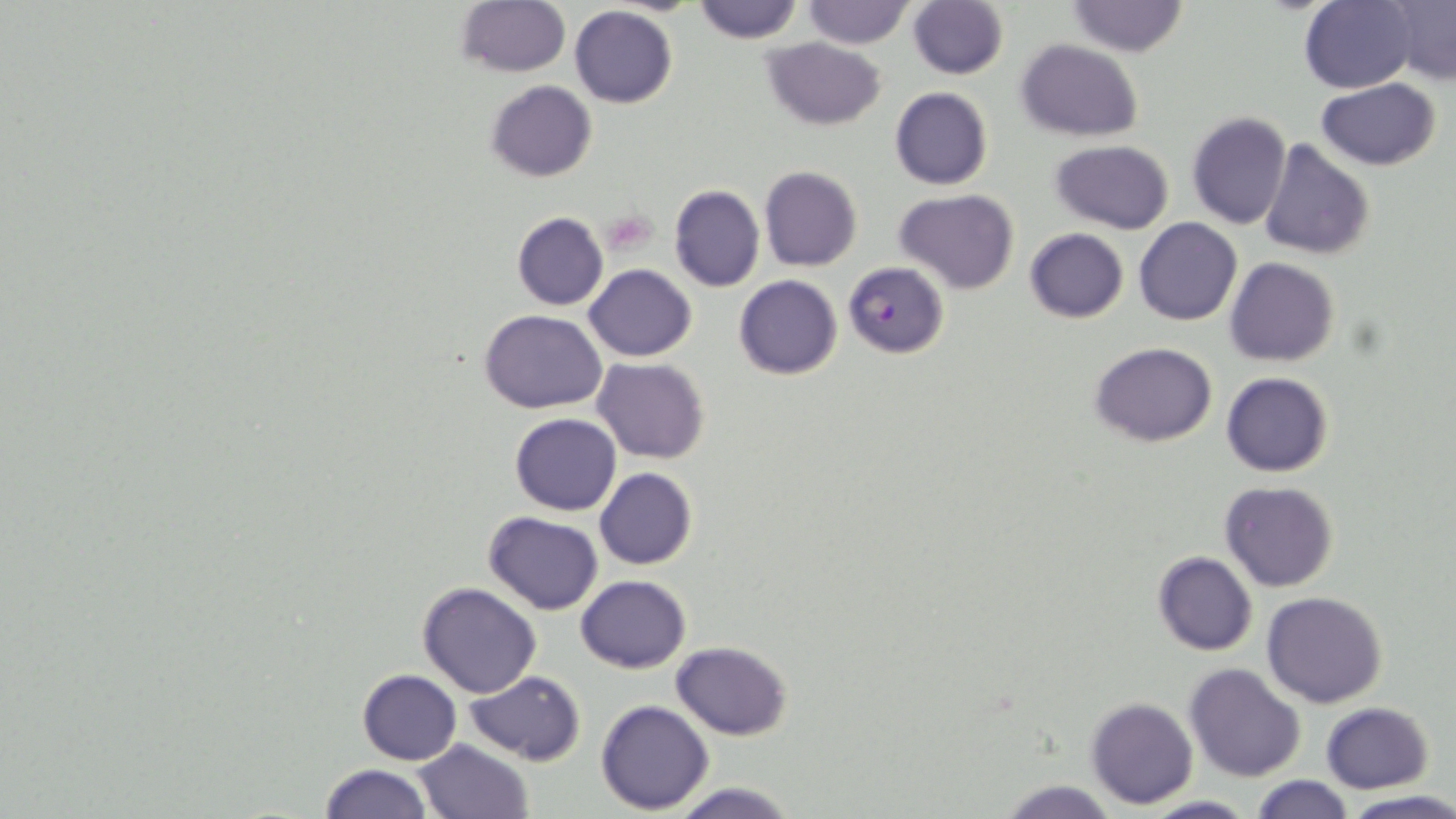

Summary:
  - Coordinate format: approximate bounding boxes as [x1, y1, x2, y2] in pixels
  - Uninfected red blood cell locations: [455, 0, 570, 79], [691, 0, 804, 43], [799, 0, 914, 47], [908, 0, 1007, 79], [1301, 0, 1418, 93], [1383, 0, 1456, 86], [1065, 1, 1189, 56], [569, 6, 677, 109], [763, 39, 885, 130], [1015, 40, 1143, 141], [1315, 79, 1442, 170], [485, 80, 597, 182], [891, 87, 993, 190], [1187, 112, 1292, 228], [1259, 138, 1375, 261], [1051, 140, 1175, 233], [760, 167, 862, 271], [668, 184, 764, 293], [894, 190, 1019, 293], [512, 212, 608, 311], [1134, 217, 1242, 325], [1024, 228, 1129, 324], [1224, 256, 1341, 367], [584, 265, 697, 362], [733, 275, 842, 380], [480, 310, 607, 414], [1091, 343, 1216, 446], [593, 358, 709, 463], [1221, 372, 1333, 476], [510, 413, 621, 515], [595, 467, 697, 569], [1220, 480, 1338, 592], [483, 511, 603, 614], [1151, 551, 1257, 656], [575, 575, 691, 672], [417, 583, 542, 698], [1262, 591, 1389, 708], [671, 641, 794, 740], [1185, 664, 1305, 783], [357, 669, 461, 765], [465, 670, 586, 765], [1087, 697, 1198, 808], [596, 699, 714, 816], [1321, 702, 1433, 794], [413, 739, 533, 819], [320, 763, 433, 819], [1248, 776, 1356, 818], [994, 779, 1125, 819], [664, 780, 805, 819], [1338, 791, 1456, 818], [1136, 797, 1260, 818]
  - Platelet locations: [603, 211, 656, 253]
  - Plasmodium falciparum-infected red blood cell locations: [843, 262, 949, 358]
  - Slide-level diagnosis: Plasmodium falciparum
  - Stain: May-Grünwald-Giemsa
  - Image size: 1456×819 pixels
  - Modality: light microscopy
  - Magnification: 1000x
  - Field of view: one of a larger specimen
  - Preparation: thin blood smear